Identify the parasite.
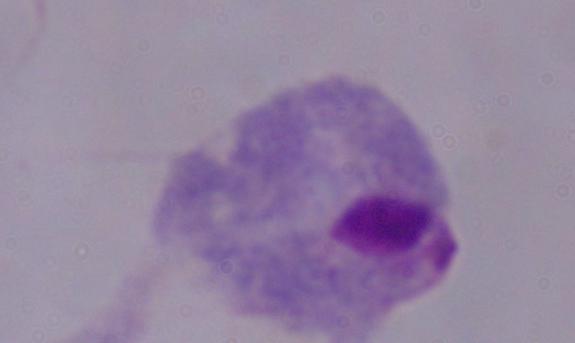
This is a trichomonad.

Photomicrograph. 1000x magnification.